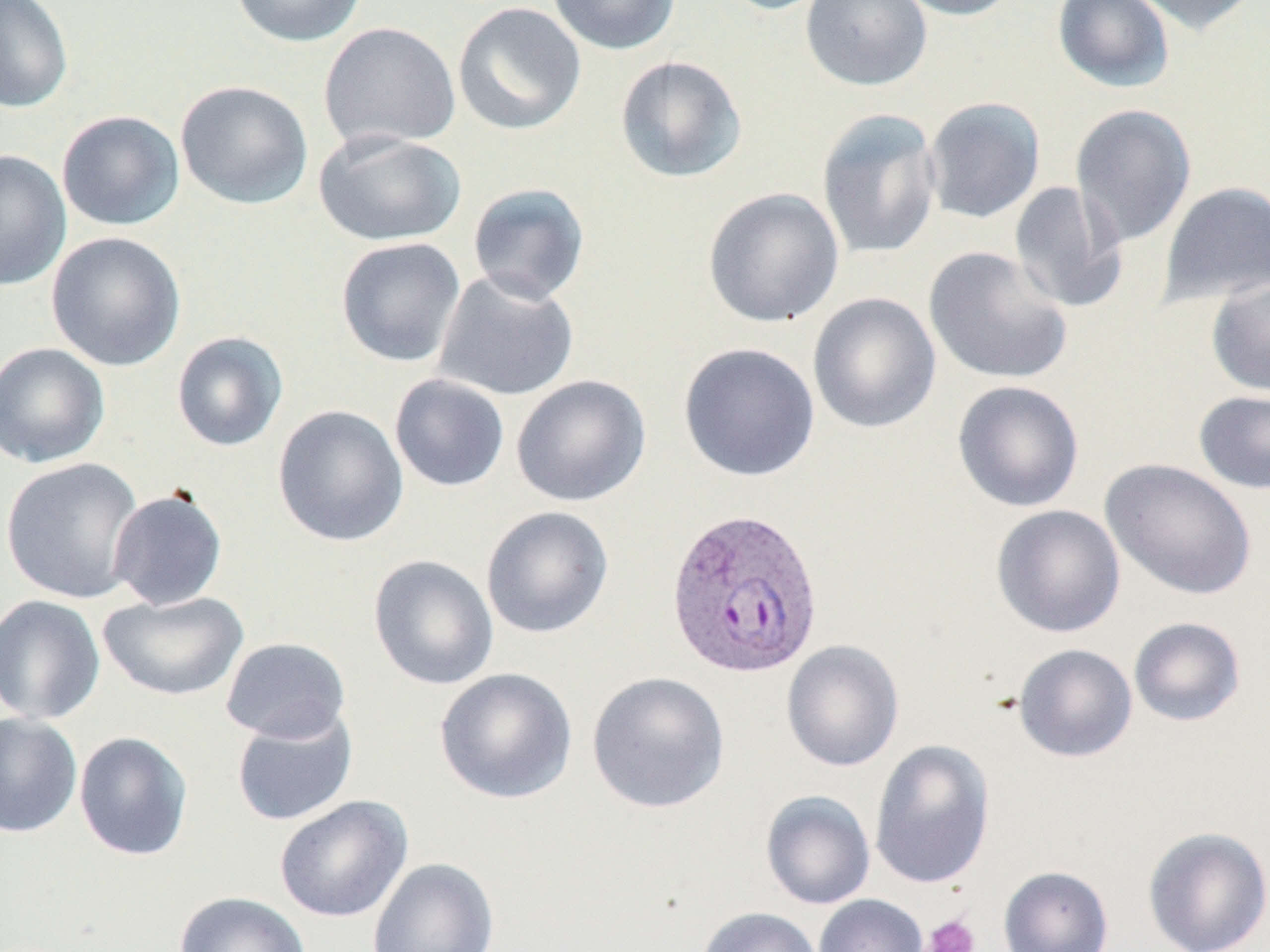
{
  "slide_level_diagnosis": "Plasmodium vivax",
  "preparation": "thin blood smear",
  "image_size": "1270×952 pixels",
  "plasmodium_vivax_infected_red_blood_cell_locations": "approximate bounding boxes as [x1, y1, x2, y2] in pixels: [665, 508, 825, 680]",
  "platelet_locations": "approximate bounding boxes as [x1, y1, x2, y2] in pixels: [920, 913, 981, 952]",
  "uninfected_red_blood_cell_locations": "approximate bounding boxes as [x1, y1, x2, y2] in pixels: [0, 0, 74, 113], [230, 0, 366, 48], [546, 0, 680, 55], [713, 0, 835, 15], [799, 0, 932, 91], [891, 0, 1023, 20], [1052, 0, 1175, 93], [1125, 0, 1262, 36], [452, 2, 586, 135], [318, 22, 461, 151], [614, 54, 748, 184], [175, 79, 314, 210], [922, 97, 1046, 224], [1070, 103, 1197, 249], [816, 107, 942, 260], [56, 110, 185, 231], [313, 130, 466, 247], [0, 150, 71, 290], [1158, 180, 1270, 308], [1009, 181, 1129, 314], [466, 182, 591, 306], [702, 187, 844, 328], [46, 231, 187, 372], [335, 237, 467, 368], [923, 246, 1073, 385], [433, 271, 579, 402], [1205, 273, 1270, 398], [807, 292, 942, 434], [171, 331, 288, 452], [0, 341, 111, 469], [678, 342, 820, 482], [388, 374, 510, 492], [511, 375, 651, 507], [952, 380, 1085, 512], [1193, 389, 1270, 495], [272, 404, 409, 547], [1, 456, 145, 604], [1100, 458, 1257, 601], [107, 488, 228, 610], [990, 504, 1126, 638], [480, 506, 614, 639], [368, 554, 499, 691], [98, 590, 249, 701], [0, 595, 106, 725], [1128, 616, 1246, 727], [220, 637, 351, 743], [781, 639, 905, 771], [1013, 643, 1138, 762], [434, 667, 578, 804], [586, 671, 730, 813], [231, 709, 358, 826], [0, 713, 82, 838], [73, 731, 193, 861], [869, 739, 995, 890], [760, 790, 876, 910], [274, 795, 413, 922], [1142, 826, 1270, 952], [367, 857, 499, 952], [998, 865, 1114, 952], [173, 891, 313, 952], [813, 894, 928, 952], [696, 906, 823, 952]",
  "modality": "optical microscopy",
  "field_of_view": "single",
  "stain": "May-Grünwald-Giemsa",
  "magnification": "1000x"
}